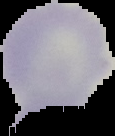

Summary:
  - Image size: 115×136 pixels
  - Malaria status: uninfected
  - Image type: segmented cell region with the area outside set to black
  - Preparation: thin blood film